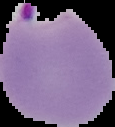

Result: malaria parasites identified. The area outside the segmented cell region is set to black. From a thin blood smear. Image is 115×127 pixels.